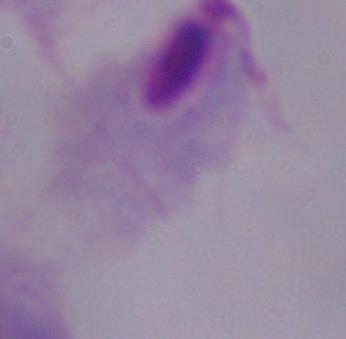 A trichomonad is seen. Micrograph. 1000x magnification.